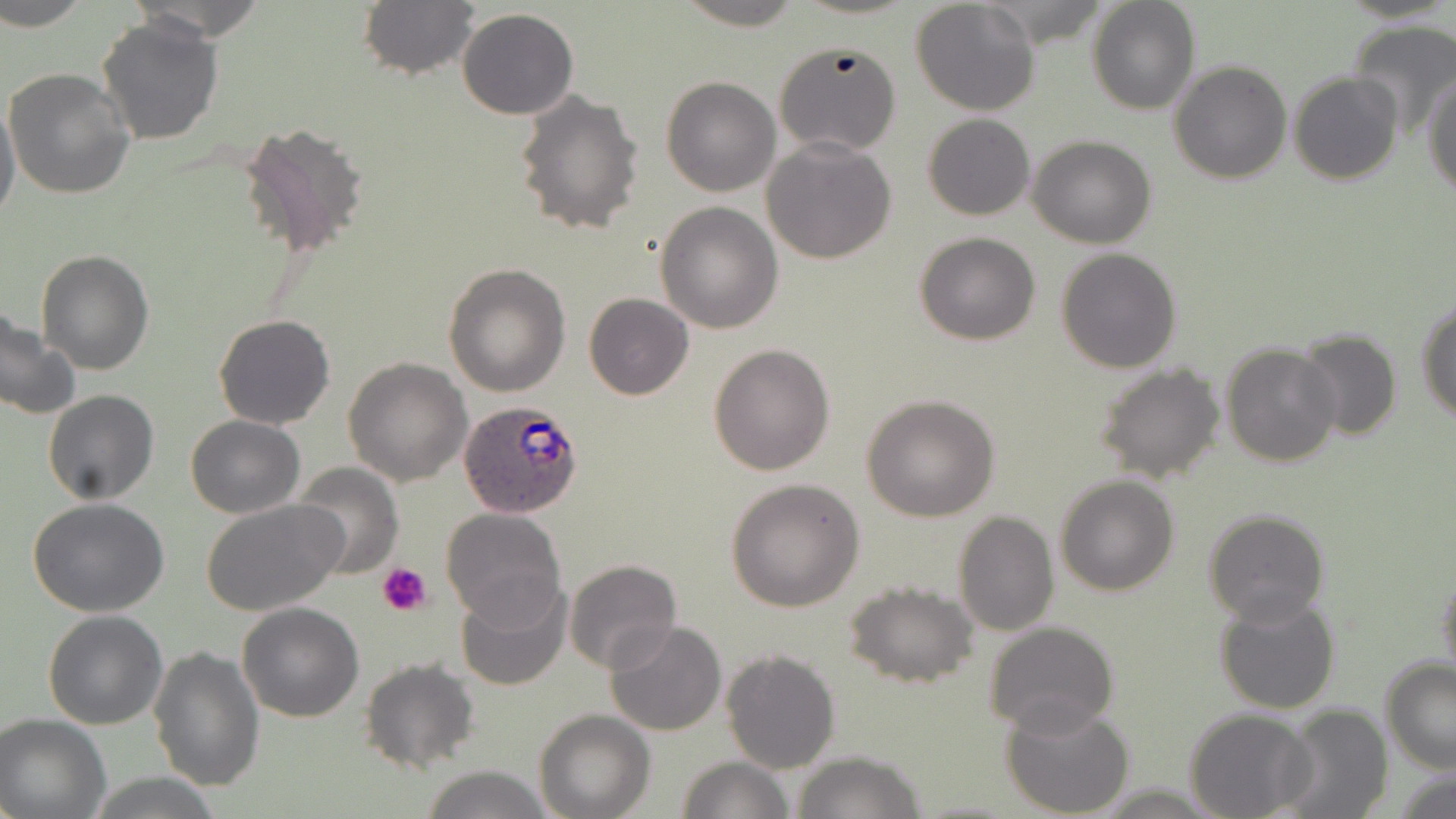

slide-level diagnosis = Plasmodium ovale
platelet locations = approximate bounding boxes as (x1, y1, x2, y2) in pixels: (378, 561, 431, 616)
image size = 1456×819 pixels
magnification = 1000x
Plasmodium ovale-infected red blood cell locations = approximate bounding boxes as (x1, y1, x2, y2) in pixels: (459, 399, 583, 515)
stain = May-Grünwald-Giemsa
preparation = thin blood film
uninfected red blood cell locations = approximate bounding boxes as (x1, y1, x2, y2) in pixels: (2, 0, 92, 31), (359, 0, 480, 80), (674, 0, 806, 30), (911, 0, 1042, 117), (1086, 0, 1201, 115), (457, 8, 579, 120), (95, 15, 224, 144), (1345, 19, 1456, 142), (773, 41, 902, 158), (1169, 61, 1292, 185), (4, 70, 135, 198), (1426, 71, 1456, 199), (1288, 73, 1401, 187), (660, 75, 782, 196), (513, 90, 645, 235), (0, 96, 21, 230), (923, 114, 1035, 221), (244, 125, 368, 260), (1029, 134, 1156, 249), (761, 137, 897, 264), (655, 201, 784, 334), (916, 232, 1041, 344), (1055, 247, 1181, 373), (35, 249, 156, 374), (442, 263, 570, 396), (584, 293, 695, 400), (1416, 298, 1456, 421), (0, 310, 78, 420), (212, 315, 335, 429), (1294, 327, 1403, 442), (709, 343, 837, 476), (1222, 343, 1343, 466), (344, 357, 472, 486), (1093, 362, 1225, 486), (43, 390, 160, 506), (861, 393, 1002, 521), (186, 416, 306, 518), (293, 463, 404, 577), (1054, 474, 1179, 595), (725, 479, 865, 612), (27, 499, 171, 617), (201, 499, 348, 615), (439, 507, 567, 627), (952, 508, 1059, 637), (1202, 508, 1330, 627), (564, 560, 682, 675), (1437, 565, 1456, 686), (455, 577, 573, 693), (844, 581, 980, 688), (1215, 594, 1341, 715), (237, 600, 365, 721), (42, 609, 168, 730), (605, 620, 728, 735), (982, 620, 1119, 736), (148, 645, 265, 790), (721, 649, 840, 774), (358, 657, 480, 773), (1381, 657, 1456, 772), (1001, 698, 1136, 818), (1274, 705, 1392, 819), (1185, 709, 1314, 819), (534, 710, 654, 819), (0, 713, 111, 818), (792, 750, 926, 819), (676, 756, 797, 818), (421, 764, 554, 819), (86, 776, 225, 816)
field of view = single
modality = optical microscopy